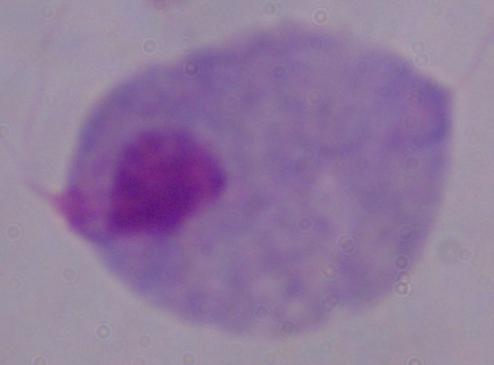
Summary:
  - Magnification: 1000x
  - Identification: trichomonad
  - Modality: micrograph